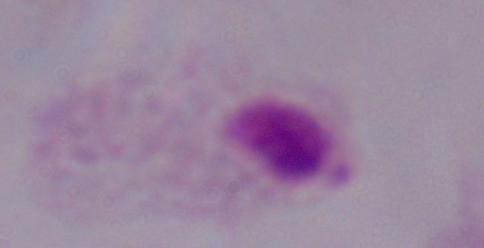
A trichomonad is shown. Captured at 1000x magnification. Photomicrograph.